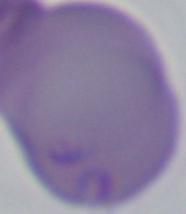

A Babesia parasite is seen. Micrograph. 1000x magnification.